Report the malaria status of this cell.
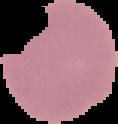

It is uninfected.

image_size: 118×124 pixels
preparation: thin blood film
image_type: segmented cell region with the area outside set to black